Assess the morphology of the erythrocytes.
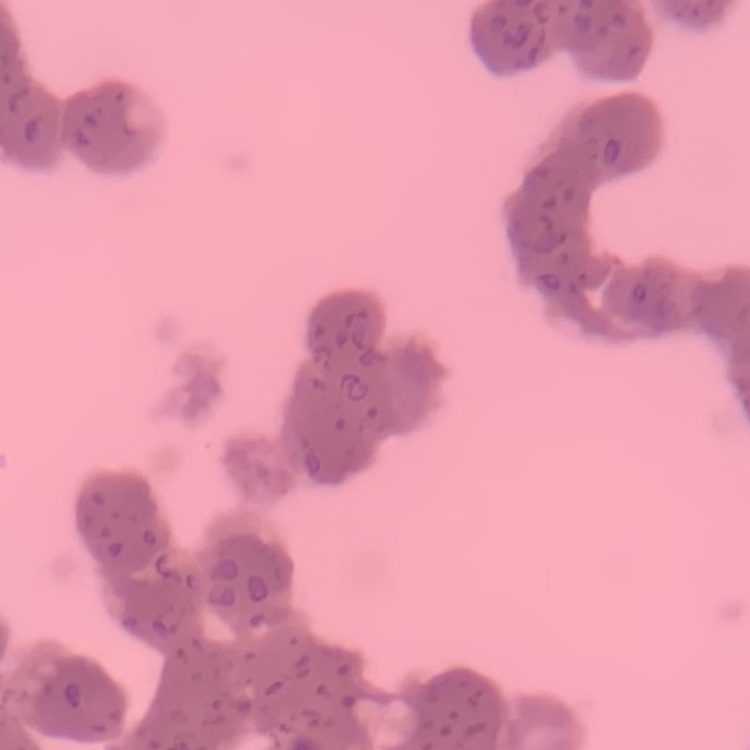

They show rouleaux formation.

Summary:
  - Preparation: thin blood film
  - Stain: Field's or Giemsa
  - Image type: one tile cut from a larger photomicrograph